Locate and identify every blood parasite.
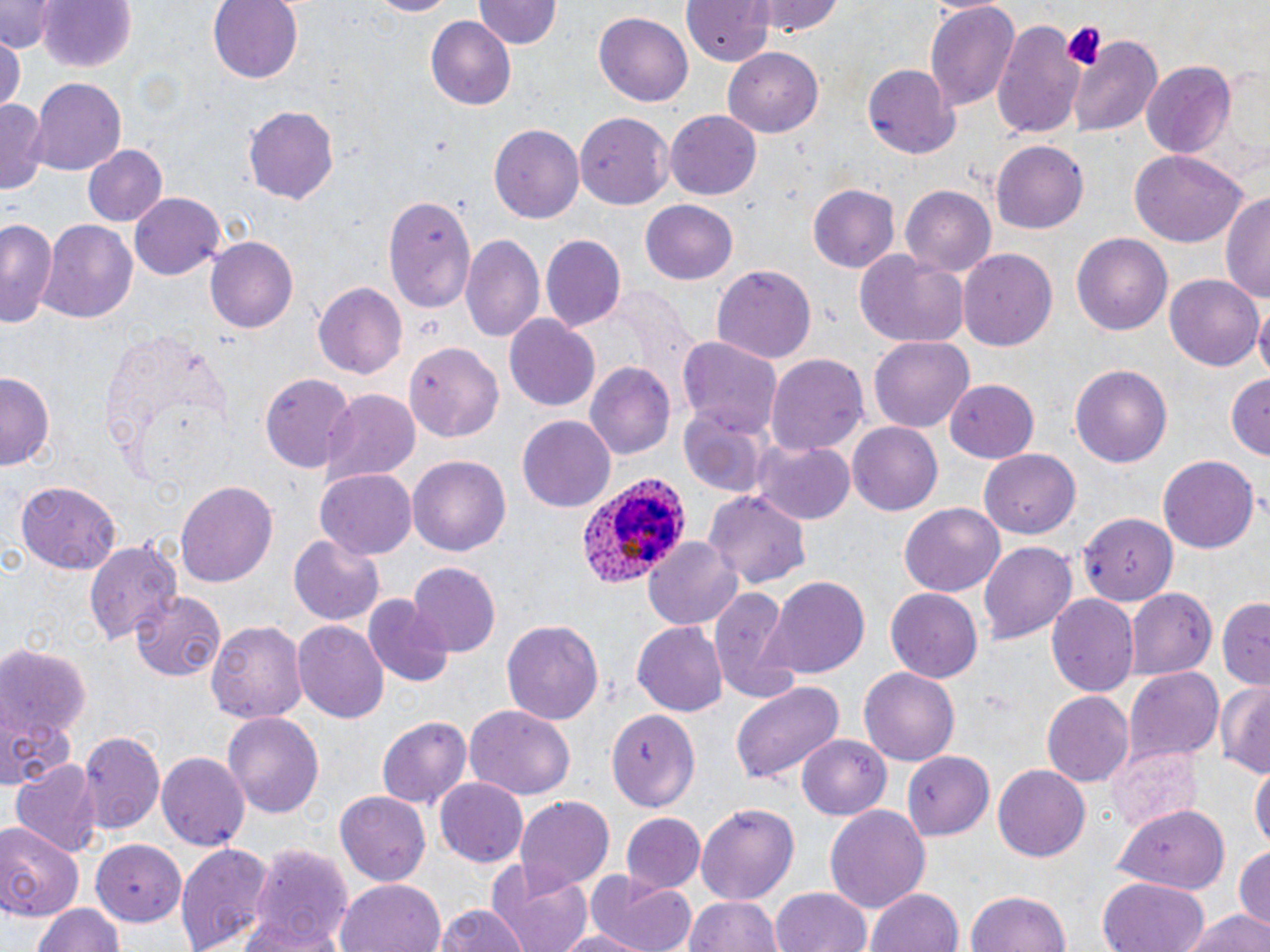
Approximate bounding boxes as (x1, y1, x2, y2) in pixels.
Plasmodium ovale-infected red blood cells: (578, 477, 690, 589).
No Plasmodium falciparum, Plasmodium malariae, Plasmodium vivax, Babesia divergens, or Trypanosoma brucei observed.

Uninfected red blood cell locations: (1, 0, 58, 51), (208, 0, 304, 84), (365, 0, 464, 18), (476, 0, 559, 51), (680, 0, 775, 66), (753, 0, 842, 36), (924, 0, 1019, 110), (37, 1, 136, 74), (594, 11, 692, 106), (424, 14, 515, 107), (991, 21, 1085, 139), (1069, 34, 1163, 137), (0, 36, 23, 113), (724, 48, 824, 137), (1141, 63, 1234, 158), (864, 67, 958, 160), (31, 79, 126, 176), (0, 98, 44, 193), (243, 104, 339, 206), (665, 110, 762, 200), (575, 114, 674, 209), (488, 123, 585, 222), (993, 140, 1089, 231), (83, 145, 167, 229), (1129, 149, 1247, 248), (808, 184, 900, 271), (900, 186, 997, 277), (1221, 189, 1270, 307), (129, 192, 228, 280), (382, 196, 475, 312), (641, 200, 739, 285), (1, 219, 60, 331), (39, 219, 139, 324), (460, 232, 542, 342), (1072, 233, 1171, 335), (205, 236, 298, 333), (540, 236, 624, 331), (959, 247, 1058, 353), (853, 251, 972, 350), (710, 265, 816, 364), (1165, 274, 1264, 372), (313, 283, 407, 381), (1256, 305, 1270, 385), (504, 315, 599, 412), (869, 334, 975, 432), (677, 336, 783, 438), (404, 341, 504, 441), (766, 354, 868, 459), (585, 363, 675, 461), (1070, 365, 1172, 468), (0, 372, 52, 470), (261, 373, 356, 475), (1226, 373, 1270, 461), (945, 380, 1040, 464), (320, 390, 420, 483), (677, 411, 769, 498), (517, 416, 616, 512), (848, 422, 942, 516), (755, 441, 854, 526), (979, 448, 1078, 535), (1157, 455, 1259, 554), (408, 456, 511, 555), (315, 468, 418, 558), (175, 480, 278, 590), (13, 481, 121, 574), (705, 489, 810, 588), (899, 502, 1006, 600), (1079, 513, 1178, 605), (289, 535, 384, 625), (644, 537, 742, 631), (82, 538, 181, 646), (978, 541, 1077, 646), (407, 562, 500, 655), (764, 575, 869, 678), (1125, 587, 1217, 679), (885, 588, 983, 683), (133, 590, 226, 680), (710, 590, 798, 702), (1047, 592, 1138, 699), (362, 594, 453, 687), (1217, 598, 1268, 687), (501, 617, 604, 728), (205, 618, 308, 725), (294, 619, 388, 724), (631, 623, 726, 717), (0, 645, 89, 740), (858, 667, 961, 766), (1125, 669, 1223, 762), (1215, 679, 1270, 776), (730, 681, 846, 786), (1041, 691, 1134, 788), (465, 705, 575, 799), (0, 708, 74, 790), (607, 708, 701, 812), (224, 712, 325, 819), (375, 715, 471, 809), (79, 730, 164, 836), (798, 736, 890, 819), (1107, 741, 1202, 831), (157, 751, 249, 852), (902, 751, 995, 840), (12, 760, 102, 856), (1251, 763, 1269, 855), (992, 764, 1090, 863), (434, 778, 528, 869), (336, 791, 429, 886), (514, 795, 613, 894), (697, 803, 800, 902), (825, 805, 931, 911), (1112, 805, 1228, 893), (621, 811, 705, 894), (0, 820, 82, 920), (90, 839, 185, 922), (174, 841, 274, 952), (246, 842, 352, 952), (1233, 843, 1269, 924), (485, 859, 595, 952), (587, 871, 696, 952), (1097, 877, 1208, 952), (335, 878, 445, 952), (770, 887, 873, 952), (864, 887, 966, 952), (962, 888, 1076, 952), (685, 895, 783, 952), (31, 902, 123, 952), (433, 903, 533, 952), (1178, 910, 1269, 952), (551, 929, 650, 952). Platelet locations: (1060, 20, 1108, 70). Slide-level diagnosis: Plasmodium ovale. Light microscopy. Image is 1270×952 pixels. May-Grünwald-Giemsa stain. 1000x magnification. Thin blood smear. One field of a larger specimen.